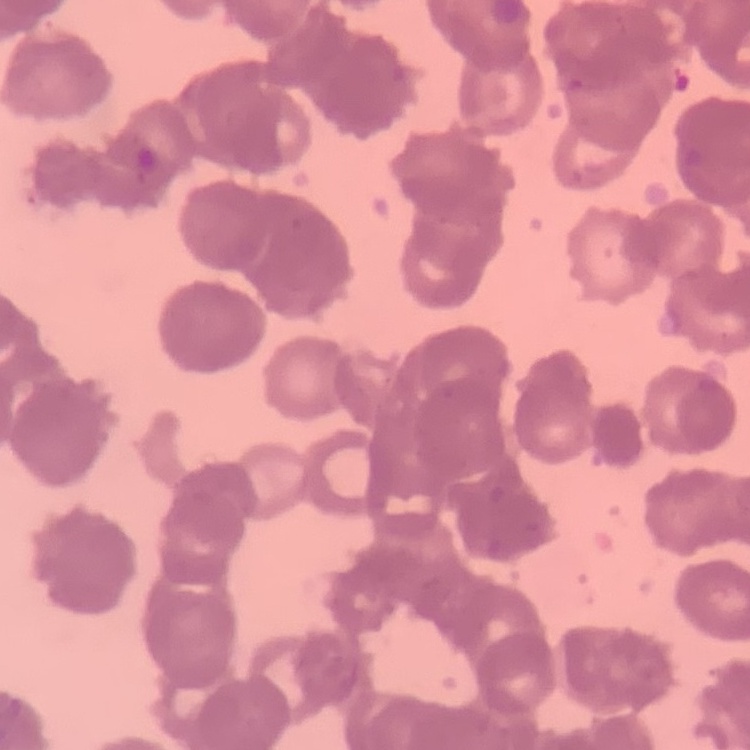
The erythrocytes exhibit rouleaux formation. Field's or Giemsa stain. Thin peripheral smear. One tile cut from a larger photomicrograph.